Give the position of every Plasmodium parasite and every leukocyte.
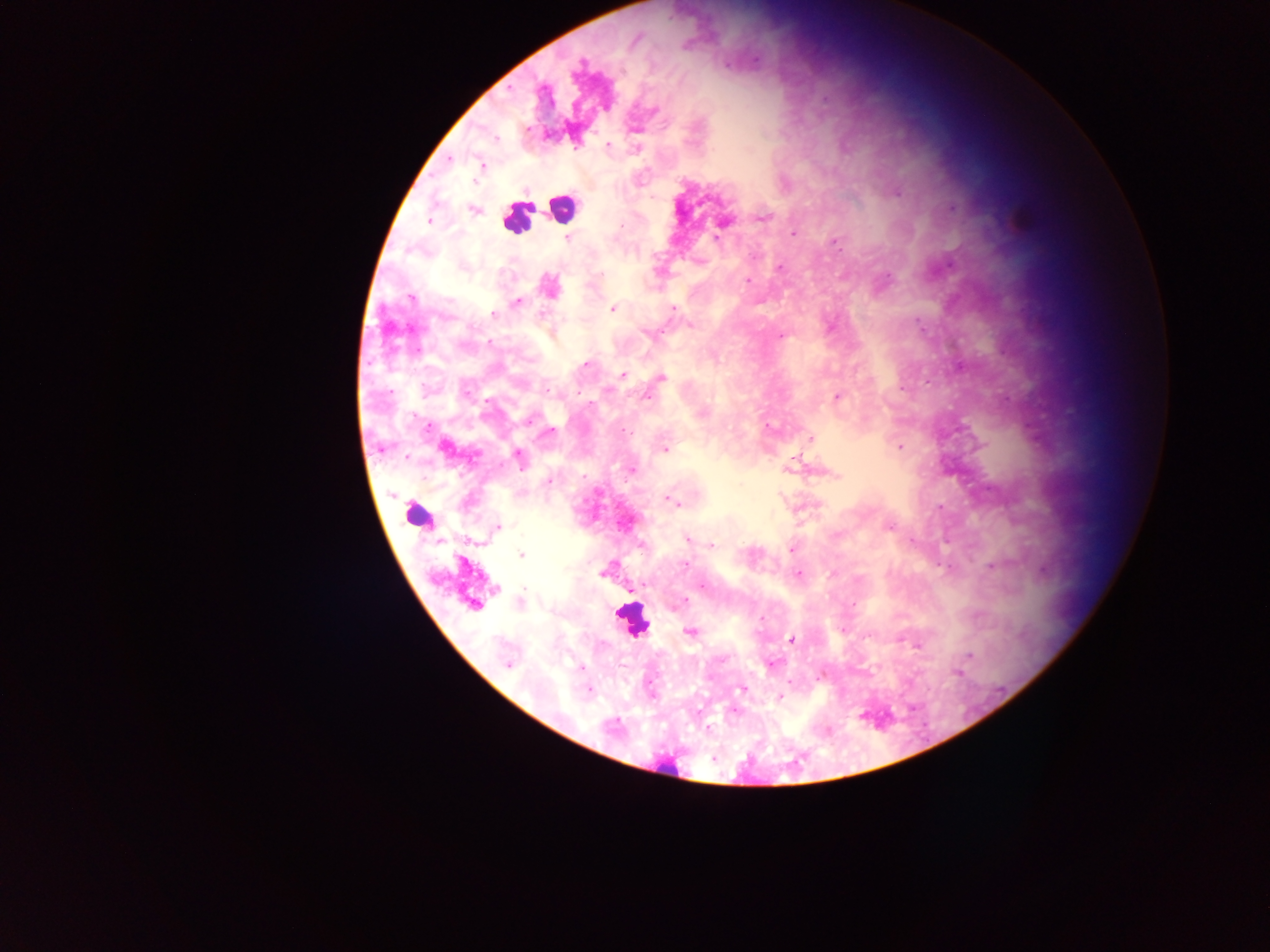
Approximate centers as [x, y] in pixels.
Plasmodium parasites: [581, 64], [653, 109], [608, 144], [713, 151], [481, 166], [475, 181], [897, 192], [952, 208], [473, 210], [763, 217], [1022, 218], [429, 220], [723, 223], [794, 233], [717, 237], [568, 238], [835, 244], [780, 268], [599, 275], [888, 278], [748, 280], [550, 286], [411, 298], [517, 301], [672, 308], [612, 309], [493, 314], [690, 324], [649, 334], [780, 335], [586, 364], [623, 374], [662, 377], [903, 389], [647, 396], [837, 397], [530, 420], [769, 427], [549, 431], [811, 438], [900, 446], [445, 448], [666, 449], [519, 457], [632, 469], [837, 475], [549, 482], [669, 500], [940, 506], [499, 527], [889, 527], [687, 539], [911, 541], [712, 545], [791, 549], [522, 555], [463, 564], [684, 565], [991, 565], [604, 572], [798, 573], [832, 574], [702, 586], [521, 602], [684, 602], [473, 605], [761, 619], [690, 633], [792, 640], [917, 646], [969, 655], [772, 665], [507, 666], [582, 668], [956, 673], [742, 689], [589, 690], [780, 697].
Leukocytes: [562, 207], [516, 218], [417, 511], [632, 620].

Thick blood smear. Photographed through a microscope with a mobile-phone camera. One field of view. Image is 1270×952 pixels. Collected in Ghana.